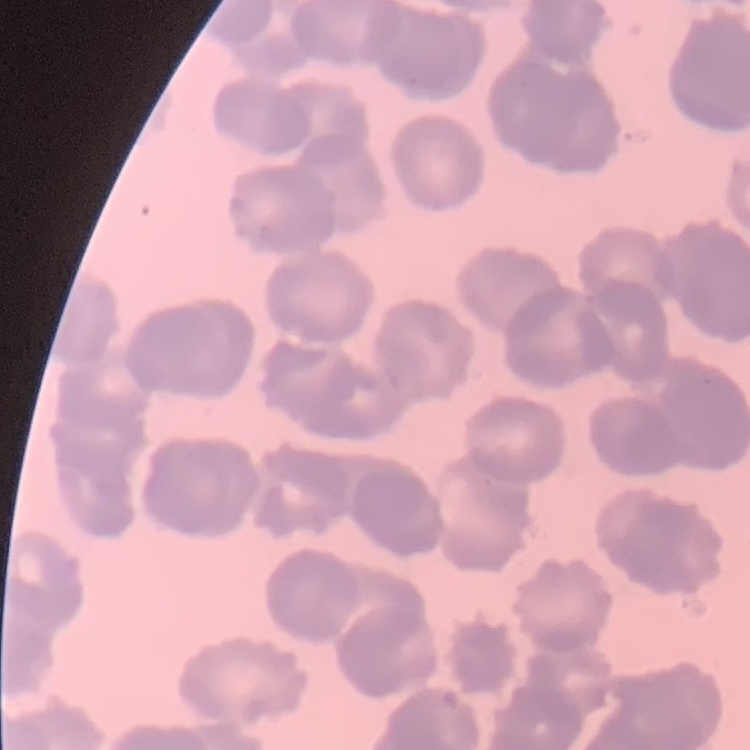
The red blood cells show rouleaux formation. Thin blood film. Stained with either Field's or Giemsa. One tile cut from a larger photomicrograph.